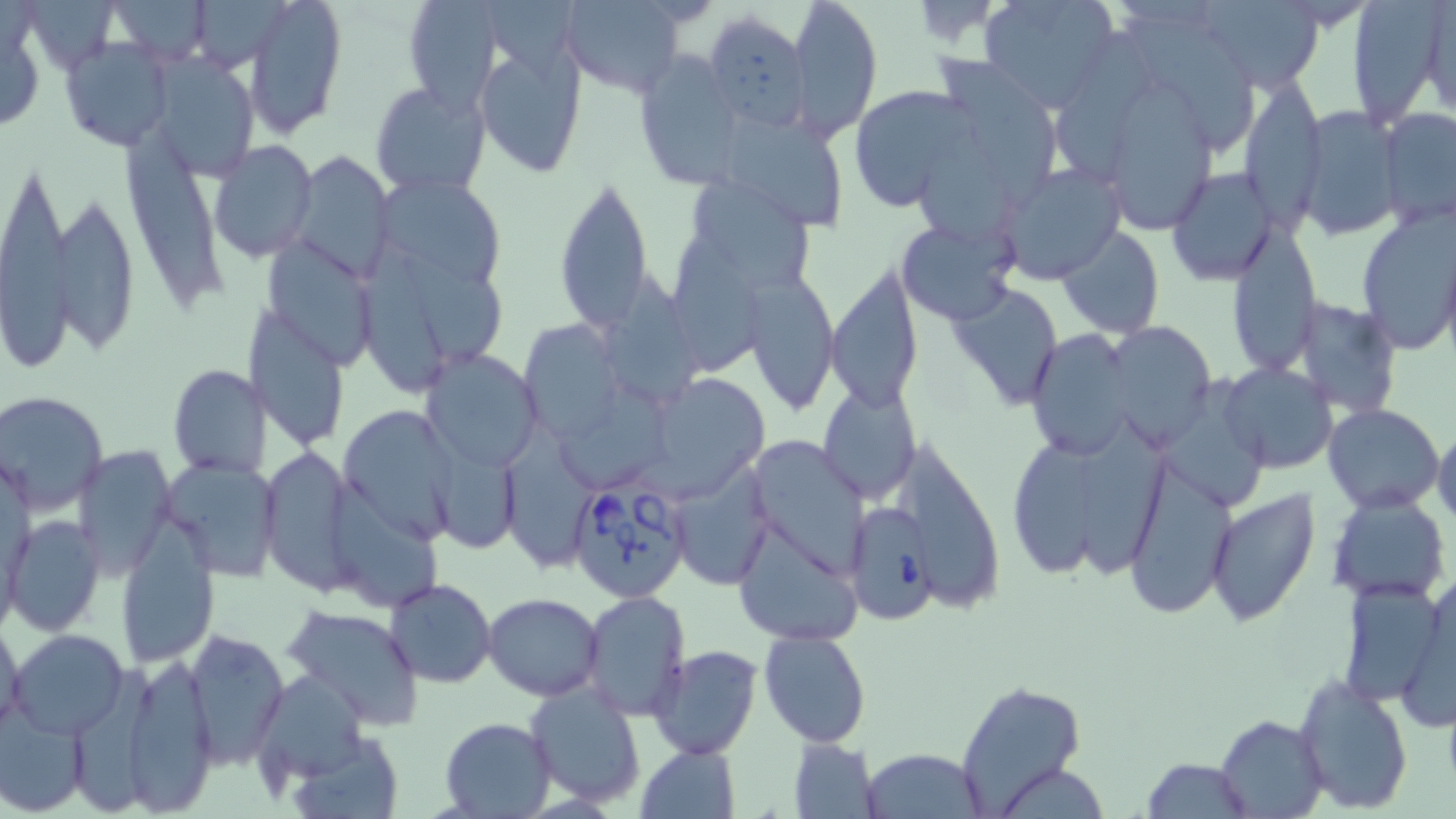

slide-level diagnosis = Babesia divergens
modality = light microscopy
preparation = thin blood smear
Babesia divergens-infected red blood cell locations = approximate bounding boxes as named x1/y1/x2/y2 corners in pixels: (x1=570, y1=476, x2=692, y2=603), (x1=846, y1=504, x2=936, y2=627)
stain = May-Grünwald-Giemsa
uninfected red blood cell locations = approximate bounding boxes as named x1/y1/x2/y2 corners in pixels: (x1=109, y1=0, x2=213, y2=63), (x1=245, y1=0, x2=348, y2=136), (x1=400, y1=0, x2=503, y2=113), (x1=788, y1=0, x2=883, y2=142), (x1=978, y1=0, x2=1117, y2=112), (x1=1345, y1=0, x2=1451, y2=128), (x1=556, y1=1, x2=691, y2=98), (x1=1190, y1=1, x2=1324, y2=88), (x1=33, y1=2, x2=118, y2=75), (x1=196, y1=3, x2=289, y2=74), (x1=1414, y1=5, x2=1454, y2=115), (x1=701, y1=12, x2=809, y2=132), (x1=1130, y1=15, x2=1260, y2=158), (x1=1055, y1=26, x2=1158, y2=178), (x1=474, y1=33, x2=589, y2=179), (x1=60, y1=37, x2=174, y2=151), (x1=631, y1=50, x2=745, y2=189), (x1=939, y1=52, x2=1061, y2=208), (x1=157, y1=54, x2=258, y2=176), (x1=1238, y1=78, x2=1326, y2=229), (x1=369, y1=81, x2=489, y2=199), (x1=848, y1=83, x2=975, y2=212), (x1=1112, y1=84, x2=1216, y2=227), (x1=1294, y1=105, x2=1401, y2=239), (x1=1380, y1=107, x2=1456, y2=226), (x1=721, y1=112, x2=848, y2=233), (x1=918, y1=123, x2=1017, y2=248), (x1=122, y1=136, x2=224, y2=309), (x1=208, y1=140, x2=316, y2=262), (x1=290, y1=150, x2=395, y2=284), (x1=995, y1=162, x2=1126, y2=282), (x1=0, y1=166, x2=79, y2=370), (x1=1166, y1=168, x2=1280, y2=285), (x1=376, y1=173, x2=508, y2=289), (x1=679, y1=173, x2=820, y2=294), (x1=554, y1=174, x2=655, y2=336), (x1=50, y1=195, x2=141, y2=354), (x1=1354, y1=208, x2=1456, y2=352), (x1=897, y1=218, x2=1019, y2=325), (x1=1227, y1=225, x2=1321, y2=375), (x1=1057, y1=226, x2=1165, y2=338), (x1=673, y1=235, x2=769, y2=373), (x1=264, y1=239, x2=379, y2=371), (x1=399, y1=244, x2=504, y2=364), (x1=361, y1=266, x2=443, y2=393), (x1=826, y1=266, x2=922, y2=413), (x1=609, y1=272, x2=705, y2=406), (x1=745, y1=275, x2=841, y2=415), (x1=950, y1=284, x2=1064, y2=410), (x1=1290, y1=296, x2=1403, y2=418), (x1=248, y1=311, x2=348, y2=450), (x1=519, y1=320, x2=622, y2=441), (x1=1102, y1=322, x2=1214, y2=446), (x1=1027, y1=327, x2=1139, y2=460), (x1=422, y1=350, x2=542, y2=470), (x1=1217, y1=362, x2=1337, y2=475), (x1=167, y1=364, x2=271, y2=479), (x1=1166, y1=374, x2=1268, y2=513), (x1=640, y1=382, x2=765, y2=500), (x1=818, y1=383, x2=919, y2=505), (x1=551, y1=384, x2=677, y2=493), (x1=3, y1=392, x2=109, y2=515), (x1=1322, y1=404, x2=1444, y2=515), (x1=339, y1=405, x2=460, y2=543), (x1=1081, y1=415, x2=1170, y2=579), (x1=1432, y1=424, x2=1456, y2=530), (x1=502, y1=428, x2=600, y2=566), (x1=746, y1=434, x2=871, y2=578), (x1=910, y1=436, x2=1004, y2=622), (x1=1012, y1=442, x2=1099, y2=579), (x1=71, y1=447, x2=176, y2=578), (x1=441, y1=447, x2=525, y2=550), (x1=1119, y1=452, x2=1237, y2=620), (x1=159, y1=456, x2=283, y2=579), (x1=259, y1=456, x2=356, y2=593), (x1=670, y1=463, x2=774, y2=589), (x1=329, y1=481, x2=443, y2=614), (x1=1206, y1=489, x2=1321, y2=628), (x1=1329, y1=493, x2=1450, y2=602), (x1=733, y1=514, x2=862, y2=646), (x1=6, y1=516, x2=104, y2=637), (x1=117, y1=528, x2=220, y2=668), (x1=1335, y1=576, x2=1450, y2=708), (x1=385, y1=577, x2=497, y2=688), (x1=483, y1=592, x2=603, y2=702), (x1=580, y1=592, x2=691, y2=721), (x1=282, y1=604, x2=425, y2=727), (x1=0, y1=616, x2=25, y2=735), (x1=7, y1=629, x2=129, y2=739), (x1=181, y1=629, x2=290, y2=768), (x1=758, y1=629, x2=870, y2=747), (x1=650, y1=646, x2=763, y2=760), (x1=110, y1=654, x2=224, y2=814), (x1=75, y1=661, x2=152, y2=816), (x1=256, y1=669, x2=370, y2=783), (x1=1294, y1=675, x2=1413, y2=812), (x1=526, y1=680, x2=646, y2=807), (x1=957, y1=681, x2=1085, y2=817), (x1=0, y1=703, x2=89, y2=814), (x1=1215, y1=714, x2=1327, y2=819), (x1=439, y1=717, x2=557, y2=818), (x1=283, y1=730, x2=407, y2=818), (x1=788, y1=738, x2=880, y2=817), (x1=635, y1=743, x2=741, y2=819), (x1=862, y1=747, x2=985, y2=818), (x1=1142, y1=758, x2=1253, y2=818), (x1=994, y1=762, x2=1111, y2=817)
magnification = 1000x
field of view = one of a larger specimen
image size = 1456×819 pixels